Identify the preparation type.
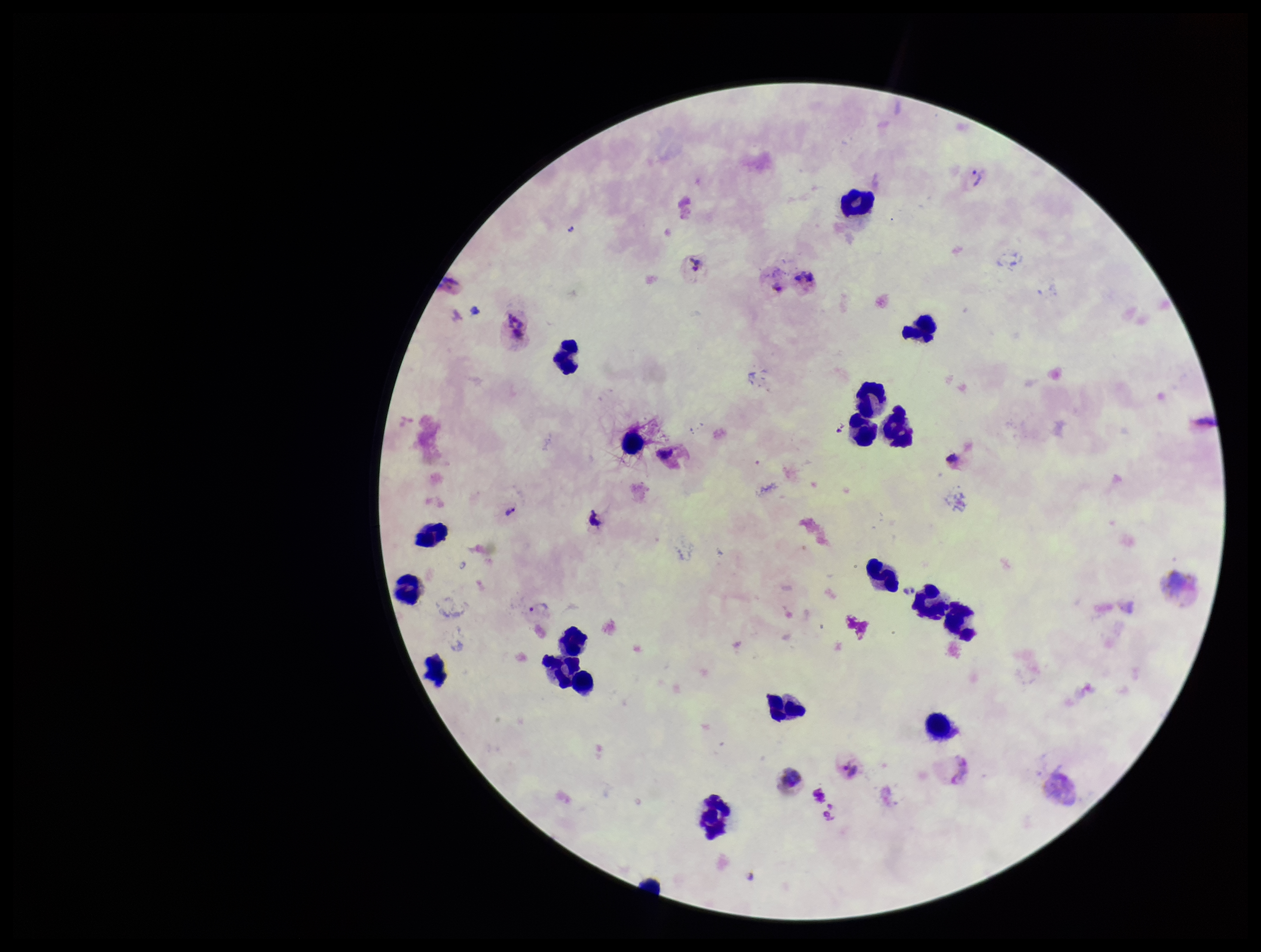
A thick smear.

parasite_count: 3
patient_malaria_status: infected
image_size: 1261×952 pixels
species_reported_for_this_patient: Plasmodium vivax
stain: Giemsa
plasmodium_parasites: seen
leukocyte_count: 21
field_of_view: one from this slide
capture: smartphone photograph through the microscope eyepiece